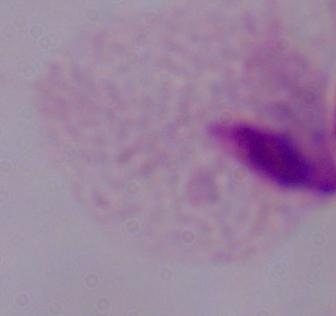
A trichomonad is shown. Captured at 1000x magnification. Photomicrograph.